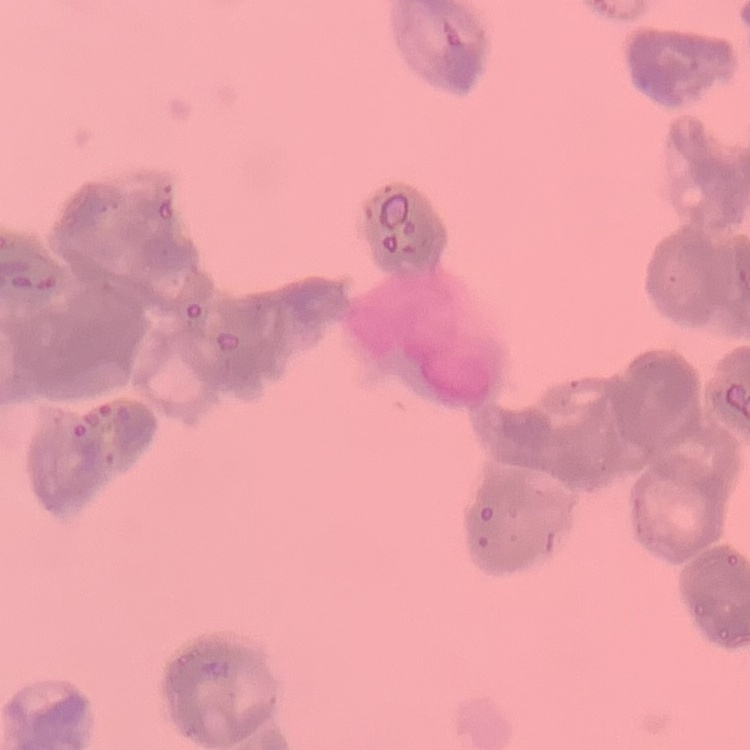
Summary:
  - Red blood cell morphology: rouleaux formation
  - Preparation: thin peripheral smear
  - Stain: Field's or Giemsa
  - Image type: one tile cut from a larger photomicrograph